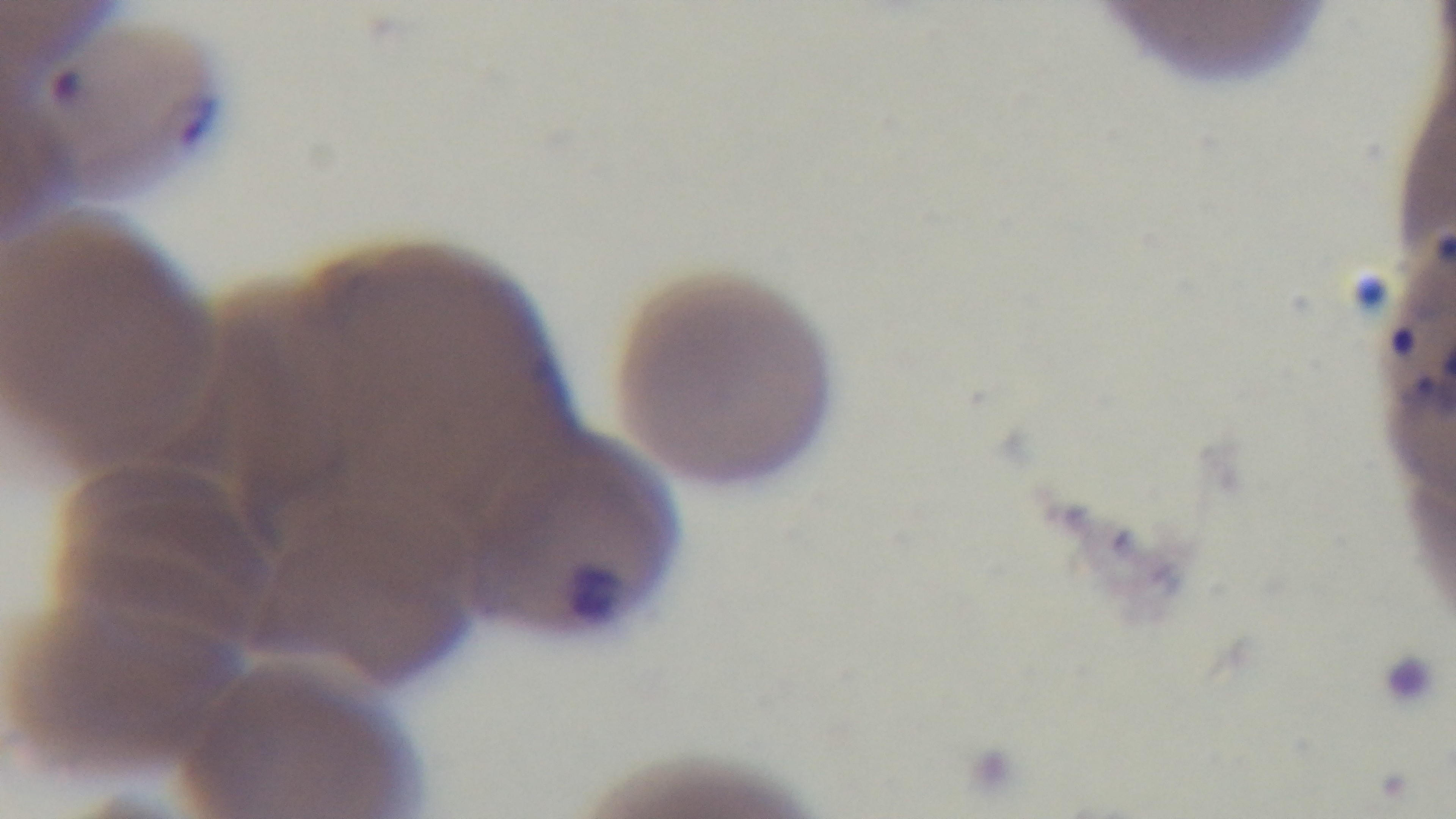 Photomicrograph. Oil-immersion objective, 100x. Mounted 4K digital camera. One field from the slide. Giemsa stain. Preparation: thin blood film. Malaria status: positive.